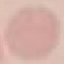

Summary:
  - Malaria status: uninfected
  - Preparation: thin smear
  - Stain: Giemsa
  - Image type: automatically extracted cell patch, resized to 64 × 64 pixels
  - Capture: smartphone through the microscope eyepiece